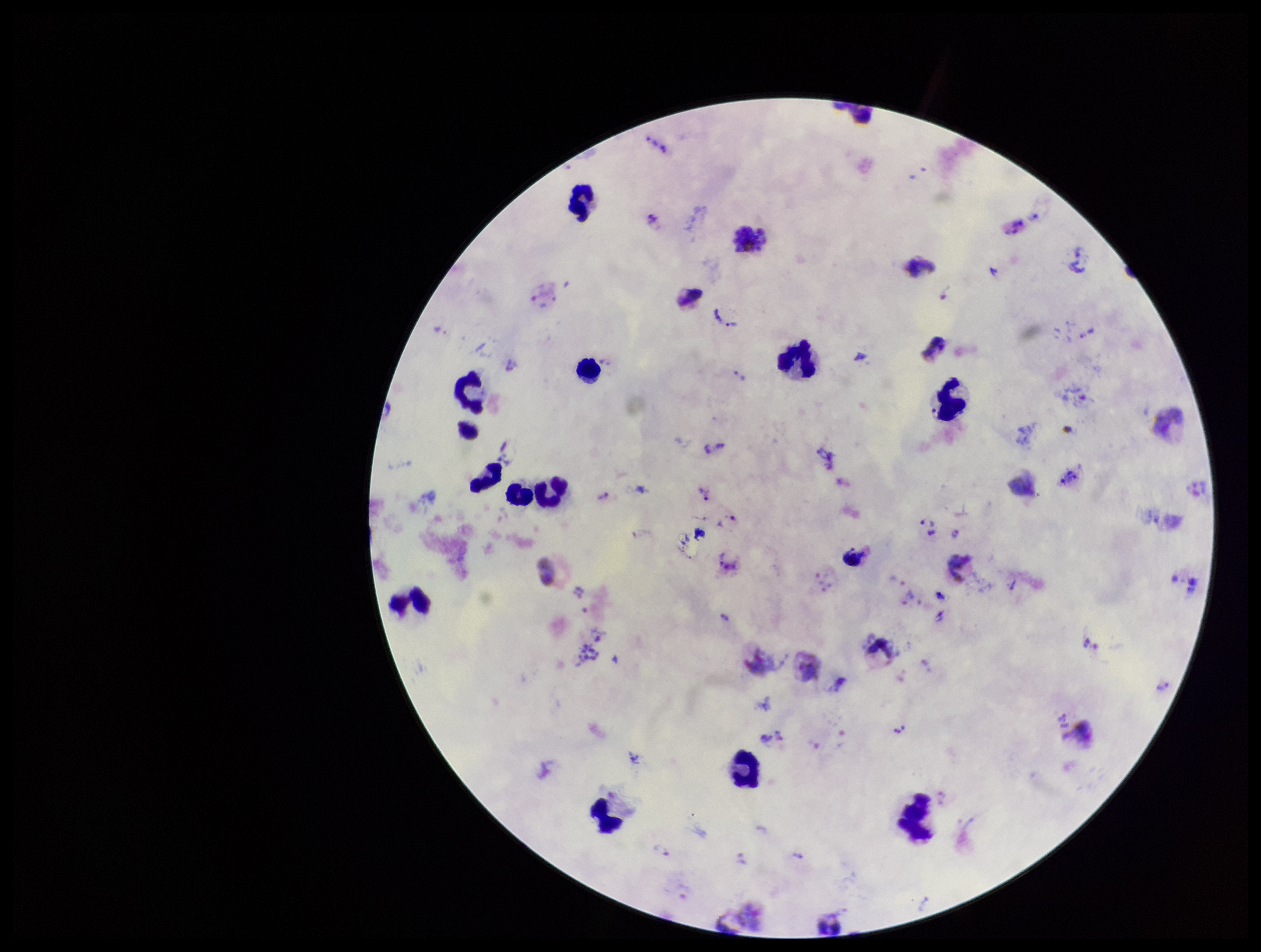

capture = smartphone photograph through the microscope eyepiece
stain = Giemsa
Plasmodium parasites = identified
field of view = single
species reported for this patient = Plasmodium vivax
patient malaria status = positive
image size = 1261×952 pixels
parasite count = 26
preparation = thick smear
leukocyte count = 16